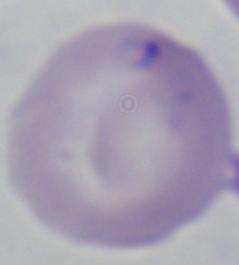

identification = Babesia
magnification = 1000x
modality = micrograph